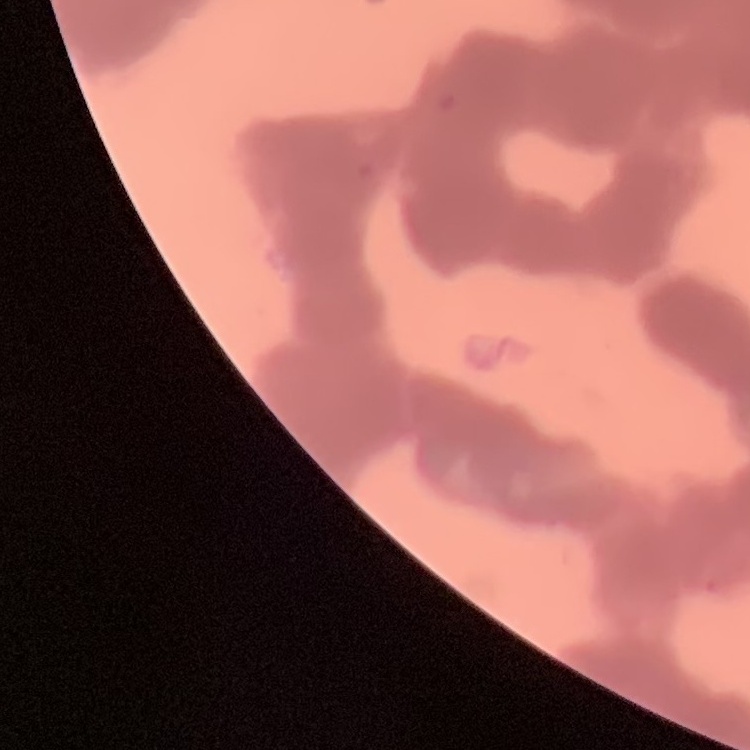

erythrocyte morphology = rouleaux formation
stain = Field's or Giemsa
preparation = thin peripheral smear
image type = one tile cut from a larger photomicrograph